Give the extent of all Plasmodium malariae-infected red blood cells.
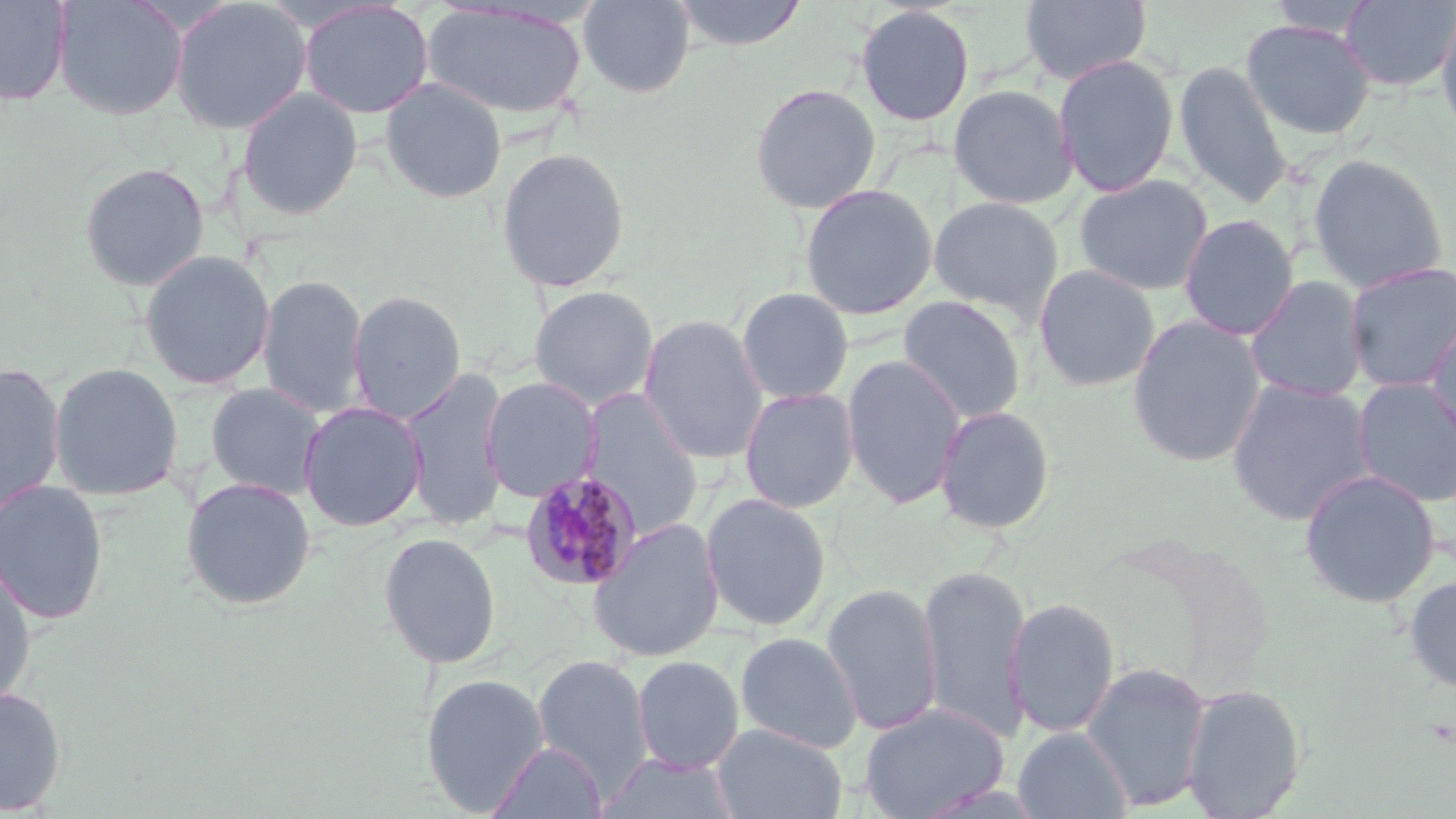

Approximate bounding boxes as (x1,y1)-(x2,y2) corner pairs in pixels.
Plasmodium malariae-infected red blood cells: (519,470)-(642,592).

{
  "slide_level_diagnosis": "Plasmodium malariae",
  "image_size": "1456×819 pixels",
  "stain": "May-Grünwald-Giemsa",
  "uninfected_red_blood_cell_locations": "approximate bounding boxes as (x1,y1)-(x2,y2) corner pairs in pixels: (0,0)-(73,106), (54,0)-(188,121), (168,0)-(313,134), (579,0)-(695,98), (672,0)-(807,51), (1020,0)-(1152,85), (1267,0)-(1377,38), (1339,0)-(1456,93), (298,1)-(434,119), (421,3)-(588,119), (1435,4)-(1456,146), (854,5)-(975,127), (1240,19)-(1376,140), (1053,53)-(1180,197), (1173,60)-(1291,208), (380,77)-(507,204), (749,83)-(881,214), (947,83)-(1078,209), (236,86)-(364,221), (495,146)-(631,293), (1308,154)-(1449,293), (77,162)-(210,293), (1074,174)-(1214,296), (799,183)-(938,320), (927,196)-(1064,324), (1178,214)-(1299,341), (139,249)-(275,390), (1342,261)-(1456,393), (1032,264)-(1160,392), (258,273)-(369,418), (1244,275)-(1370,402), (528,285)-(659,411), (736,287)-(854,405), (347,290)-(467,423), (898,295)-(1027,425), (1425,313)-(1456,449), (1126,314)-(1266,467), (638,315)-(769,465), (841,353)-(966,510), (0,360)-(66,522), (48,361)-(185,502), (399,365)-(511,531), (480,376)-(601,503), (1225,378)-(1375,526), (1352,378)-(1456,508), (204,382)-(327,501), (738,386)-(859,514), (581,388)-(705,538), (298,400)-(427,531), (935,404)-(1056,534), (1298,468)-(1440,608), (180,476)-(317,610), (0,480)-(109,625), (700,492)-(832,632), (586,518)-(725,663), (378,531)-(502,669), (0,563)-(37,709), (917,563)-(1031,741), (1403,574)-(1456,694), (821,583)-(942,736), (1005,597)-(1122,738), (735,632)-(863,753), (532,653)-(654,797), (631,655)-(744,774), (1080,661)-(1213,811), (420,672)-(550,815), (1180,683)-(1307,819), (0,686)-(68,816), (857,702)-(1010,819), (711,723)-(848,819), (1013,727)-(1133,819), (485,741)-(607,819), (595,752)-(742,819)",
  "preparation": "thin blood smear",
  "field_of_view": "one of a larger specimen",
  "modality": "optical microscopy",
  "magnification": "1000x"
}